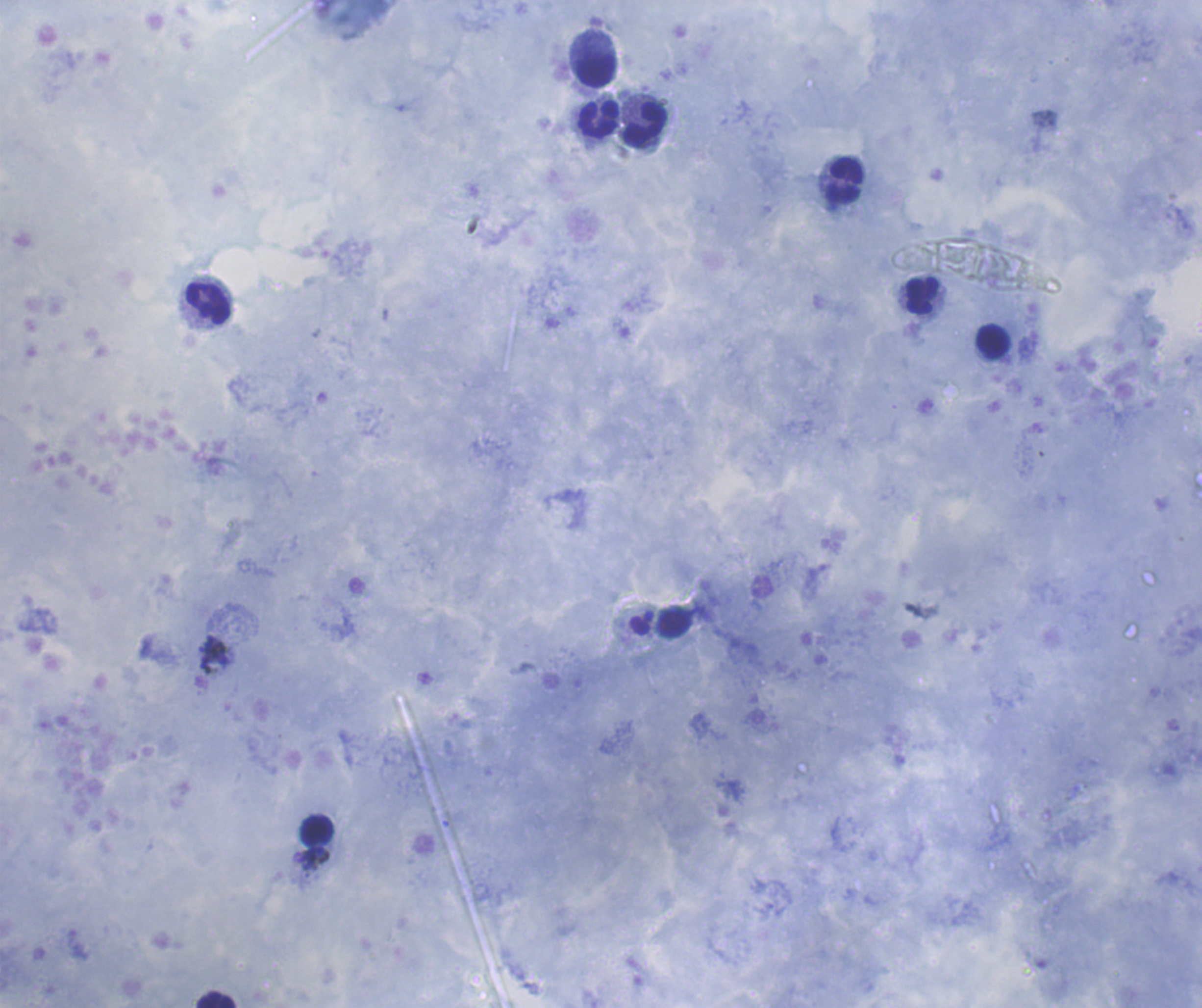
Approximate centers as (x, y) in pixels.
Summary:
  - Leukocyte locations: (597, 71), (598, 120), (645, 125), (844, 182), (921, 295), (208, 303), (992, 341), (675, 622), (317, 829), (215, 999)
  - Background quality: satisfactory
  - Magnification: 100x
  - Image size: 1202×1008 pixels
  - Result: no malaria parasites seen
  - Coloration quality: good
  - Context: previously used in an actual diagnosis
  - Field of view: single
  - Preparation: thick blood smear
  - Stain: Romanowsky